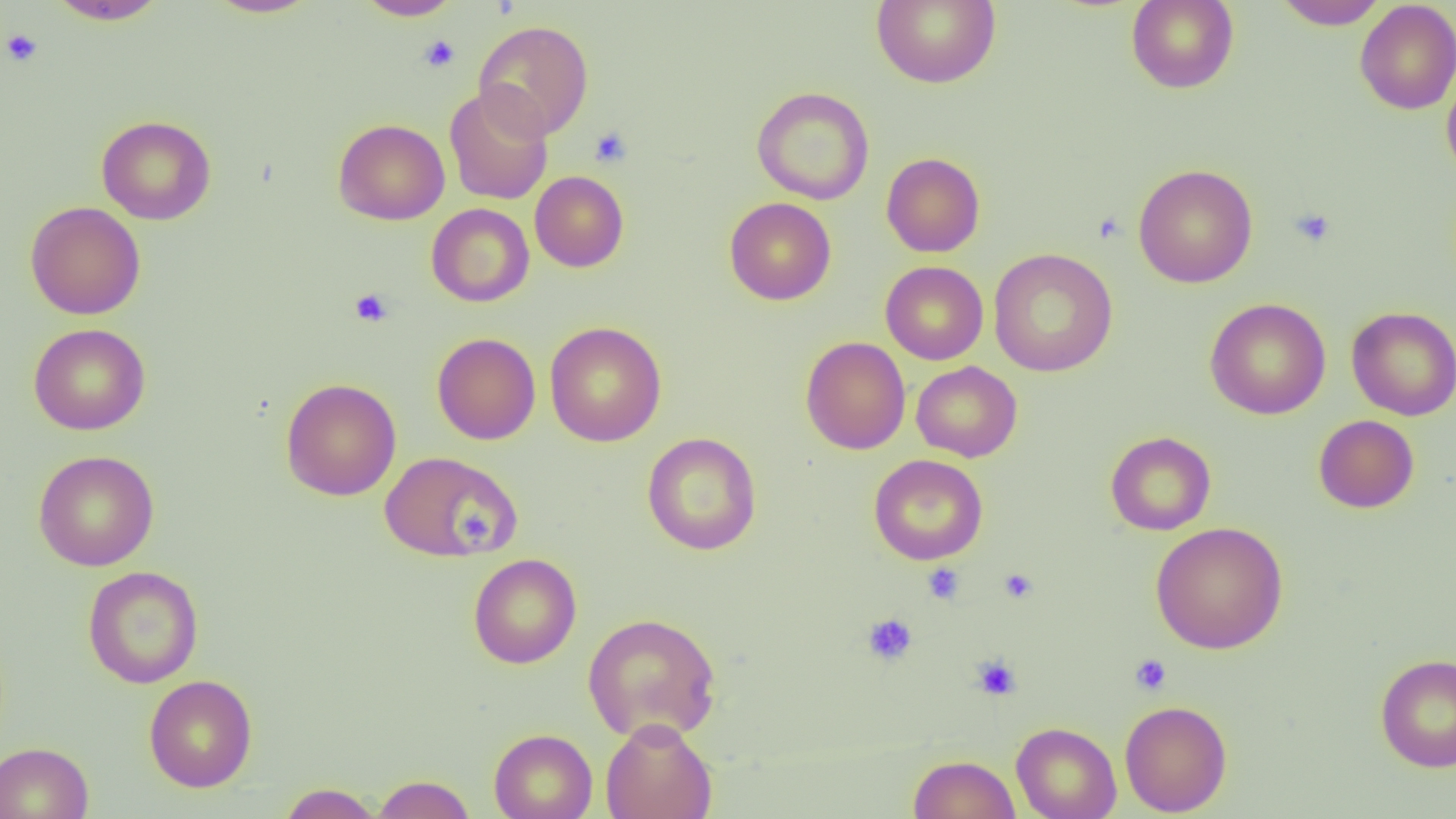

slide_level_diagnosis: no evidence of blood parasites
field_of_view: single
image_size: 1456×819 pixels
platelet_locations: 'approximate bounding boxes as named x1/y1/x2/y2 corners in pixels: (x1=1, y1=28, x2=44, y2=67), (x1=418, y1=34, x2=461, y2=72), (x1=589, y1=125, x2=633, y2=168), (x1=1289, y1=207, x2=1336, y2=248), (x1=350, y1=288, x2=393, y2=327), (x1=458, y1=510, x2=495, y2=546), (x1=922, y1=562, x2=965, y2=604), (x1=998, y1=568, x2=1038, y2=604), (x1=862, y1=612, x2=918, y2=666), (x1=1130, y1=653, x2=1172, y2=696), (x1=971, y1=655, x2=1021, y2=700)'
preparation: thin blood smear
magnification: 1000x
uninfected_red_blood_cell_locations: 'approximate bounding boxes as named x1/y1/x2/y2 corners in pixels: (x1=47, y1=0, x2=170, y2=25), (x1=204, y1=0, x2=321, y2=18), (x1=353, y1=0, x2=463, y2=20), (x1=871, y1=0, x2=1001, y2=88), (x1=1126, y1=0, x2=1239, y2=94), (x1=1272, y1=0, x2=1389, y2=30), (x1=1355, y1=1, x2=1456, y2=115), (x1=473, y1=20, x2=594, y2=141), (x1=1441, y1=69, x2=1456, y2=183), (x1=443, y1=85, x2=555, y2=205), (x1=751, y1=86, x2=875, y2=205), (x1=96, y1=115, x2=216, y2=225), (x1=333, y1=118, x2=449, y2=225), (x1=881, y1=152, x2=985, y2=257), (x1=1133, y1=164, x2=1258, y2=288), (x1=530, y1=171, x2=629, y2=272), (x1=724, y1=197, x2=836, y2=305), (x1=25, y1=202, x2=146, y2=320), (x1=426, y1=203, x2=534, y2=307), (x1=988, y1=248, x2=1118, y2=377), (x1=880, y1=261, x2=989, y2=365), (x1=1205, y1=297, x2=1331, y2=420), (x1=1346, y1=305, x2=1456, y2=421), (x1=544, y1=321, x2=667, y2=446), (x1=29, y1=323, x2=150, y2=435), (x1=432, y1=332, x2=541, y2=444), (x1=800, y1=336, x2=911, y2=454), (x1=911, y1=361, x2=1022, y2=462), (x1=280, y1=377, x2=402, y2=501), (x1=1313, y1=414, x2=1419, y2=513), (x1=1105, y1=431, x2=1216, y2=535), (x1=642, y1=432, x2=761, y2=555), (x1=32, y1=450, x2=160, y2=571), (x1=380, y1=451, x2=521, y2=563), (x1=869, y1=454, x2=988, y2=565), (x1=1149, y1=521, x2=1288, y2=653), (x1=468, y1=553, x2=581, y2=669), (x1=83, y1=565, x2=203, y2=689), (x1=582, y1=612, x2=722, y2=743), (x1=1375, y1=654, x2=1456, y2=772), (x1=143, y1=674, x2=257, y2=792), (x1=1119, y1=699, x2=1232, y2=816), (x1=601, y1=718, x2=718, y2=819), (x1=1011, y1=721, x2=1122, y2=819), (x1=489, y1=728, x2=597, y2=819), (x1=0, y1=741, x2=94, y2=819), (x1=908, y1=754, x2=1020, y2=819), (x1=372, y1=774, x2=475, y2=818), (x1=278, y1=782, x2=383, y2=818)'
modality: light microscopy